Outline each uninfected red blood cell.
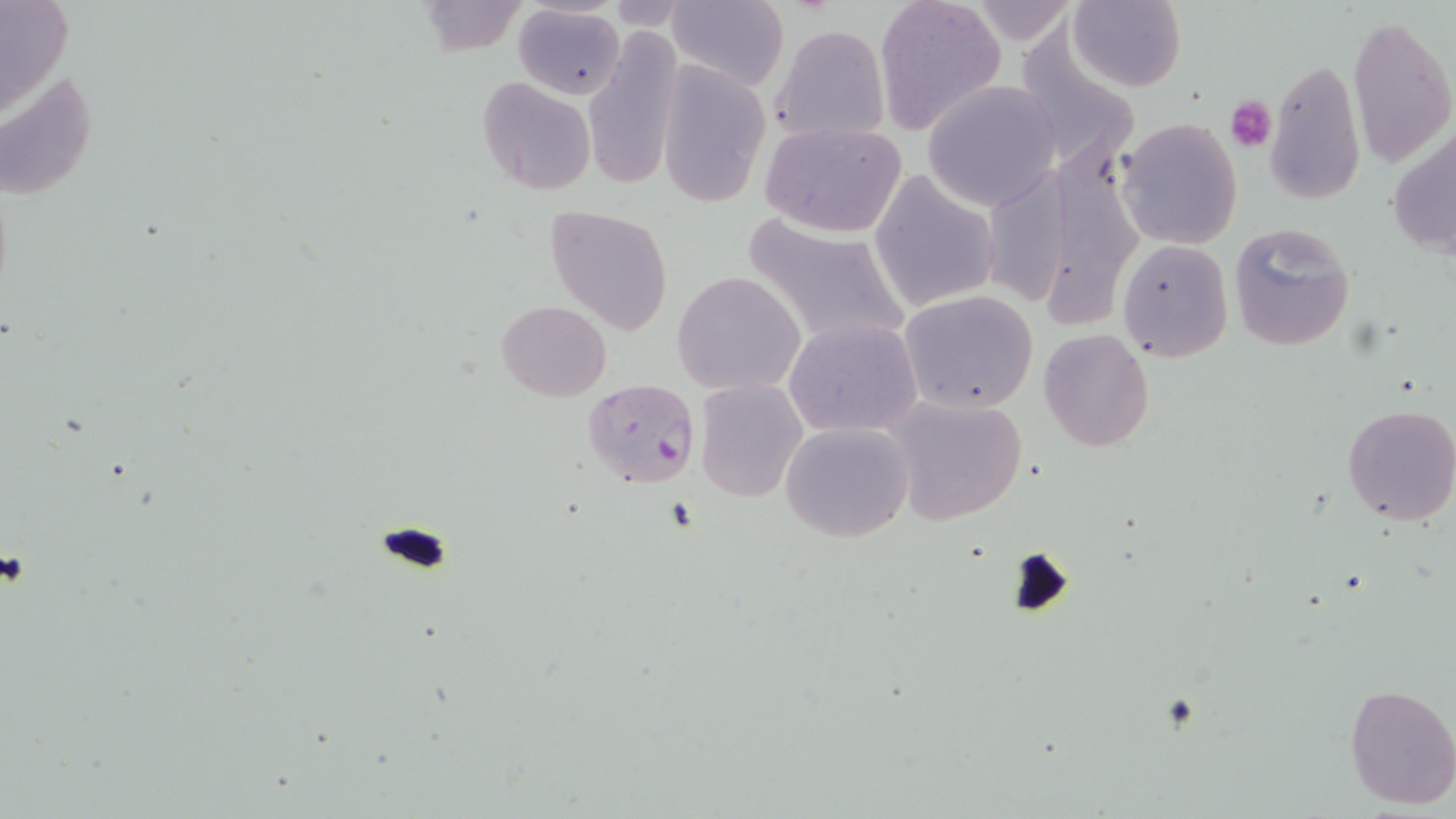
Approximate bounding boxes as named x1/y1/x2/y2 corners in pixels.
Uninfected red blood cells: (x1=1, y1=0, x2=74, y2=119), (x1=666, y1=0, x2=788, y2=92), (x1=873, y1=0, x2=1006, y2=135), (x1=1064, y1=0, x2=1188, y2=92), (x1=414, y1=2, x2=529, y2=56), (x1=514, y1=6, x2=625, y2=99), (x1=1346, y1=11, x2=1455, y2=173), (x1=1012, y1=20, x2=1136, y2=164), (x1=771, y1=25, x2=891, y2=144), (x1=582, y1=26, x2=684, y2=194), (x1=1266, y1=58, x2=1366, y2=207), (x1=657, y1=60, x2=771, y2=208), (x1=0, y1=67, x2=97, y2=205), (x1=477, y1=76, x2=596, y2=194), (x1=923, y1=81, x2=1063, y2=210), (x1=1116, y1=116, x2=1243, y2=250), (x1=1389, y1=118, x2=1456, y2=266), (x1=760, y1=121, x2=908, y2=238), (x1=1058, y1=151, x2=1149, y2=334), (x1=995, y1=155, x2=1075, y2=302), (x1=870, y1=170, x2=996, y2=314), (x1=544, y1=204, x2=674, y2=334), (x1=740, y1=212, x2=909, y2=351), (x1=1228, y1=221, x2=1356, y2=353), (x1=1117, y1=238, x2=1233, y2=362), (x1=672, y1=271, x2=806, y2=395), (x1=899, y1=290, x2=1039, y2=414), (x1=496, y1=300, x2=612, y2=401), (x1=784, y1=317, x2=922, y2=438), (x1=1039, y1=329, x2=1154, y2=451), (x1=695, y1=380, x2=808, y2=503), (x1=883, y1=391, x2=1030, y2=527), (x1=1342, y1=404, x2=1456, y2=526), (x1=780, y1=421, x2=914, y2=542), (x1=1342, y1=681, x2=1456, y2=811).

Summary:
  - Plasmodium falciparum-infected red blood cell locations: (x1=582, y1=379, x2=701, y2=491)
  - Platelet locations: (x1=1227, y1=95, x2=1276, y2=153)
  - Slide-level diagnosis: Plasmodium falciparum
  - Field of view: single
  - Stain: May-Grünwald-Giemsa
  - Image size: 1456×819 pixels
  - Preparation: thin blood film
  - Modality: optical microscopy
  - Magnification: 1000x